Assess this cell for malaria.
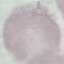

Uninfected.

Summary:
  - Stain: Giemsa
  - Image type: automatically extracted cell patch, resized to 64 × 64 pixels
  - Capture: smartphone camera at the microscope eyepiece
  - Preparation: thin smear